Report the malaria status of this cell.
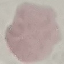

It is uninfected.

Summary:
  - Preparation: thin blood smear
  - Image type: cell patch, automatically extracted from a larger field of view and resized to 64 × 64 pixels
  - Stain: Giemsa
  - Capture: smartphone through the microscope eyepiece